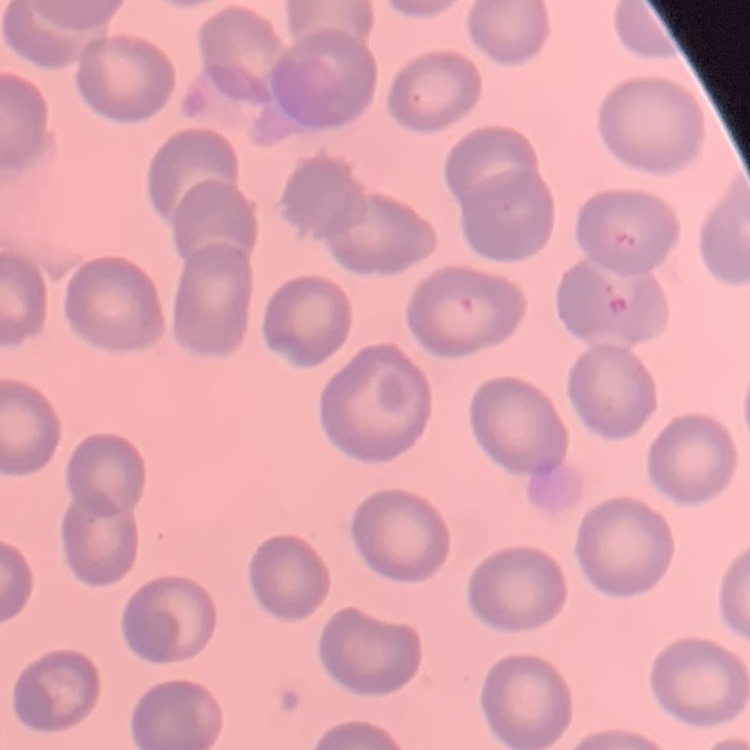
Summary:
  - Red blood cell morphology: no rouleaux formation
  - Image type: square crop of a larger photomicrograph
  - Stain: Field's or Giemsa
  - Preparation: thin blood film